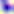

Toxoplasma gondii is shown. Photomicrograph. 400x magnification.